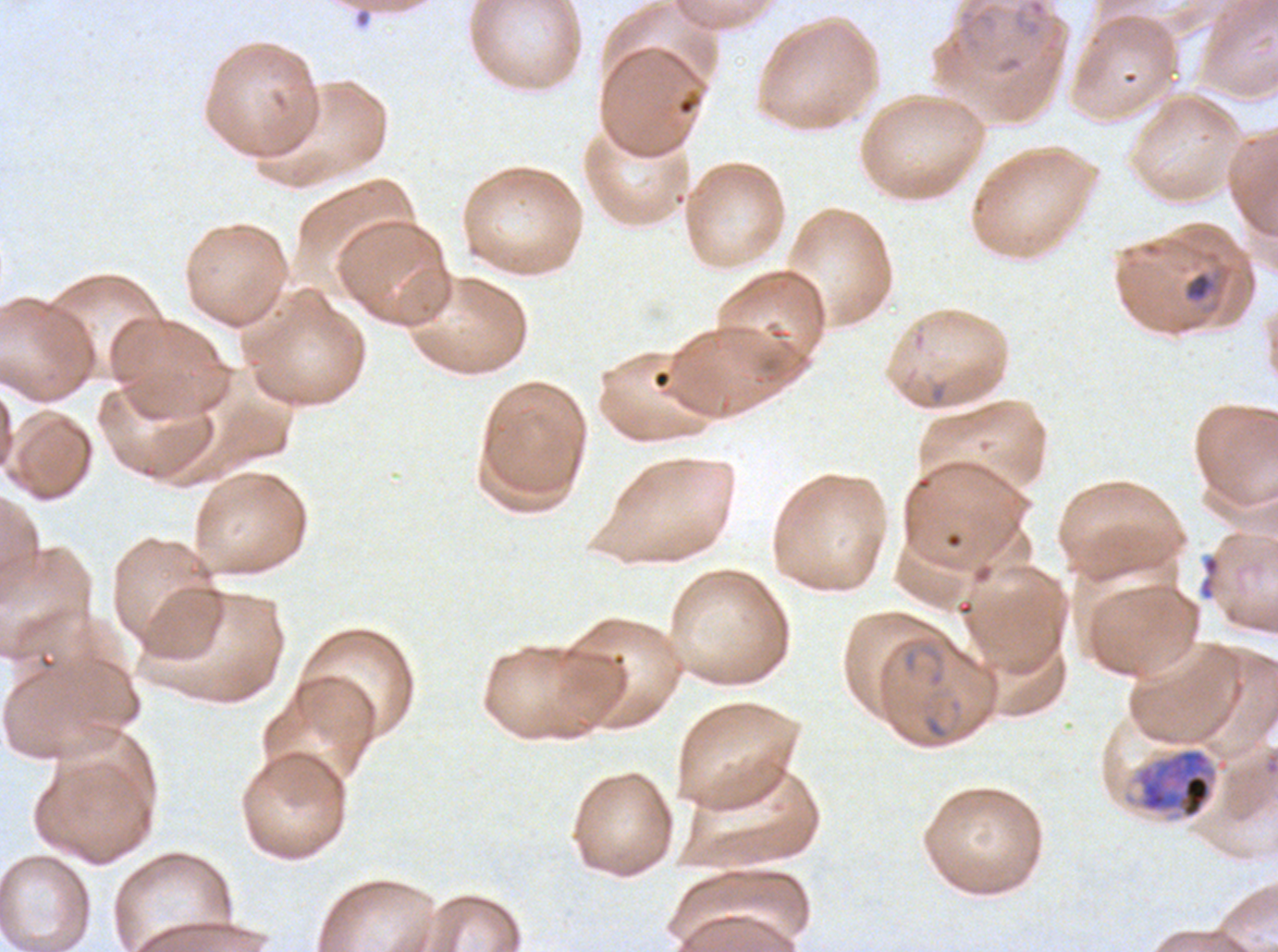
notation = approximate bounding boxes as {x1, y1, x2, y2} in pixels
early schizont locations = {1130, 747, 1230, 821}
late-ring/early-trophozoite locations = {1185, 272, 1213, 301}
debris locations = {1198, 555, 1221, 601}
ring locations = {1012, 0, 1048, 40}, {899, 637, 945, 675}
field of view = one sub-image of a larger composite
preparation = thin blood film
life-cycle stages observed = ring, late-ring/early-trophozoite, early schizont
image size = 1278×952 pixels
stain = Giemsa
specimen = Plasmodium falciparum from a patient in The Gambia, cultured ex vivo for 24 to 48 hours